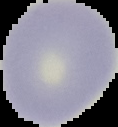
The area outside the segmented cell region is set to black. From a thin blood smear. Image is 118×127 pixels. Malaria status: uninfected.